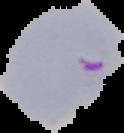

{
  "image_size": "124×133 pixels",
  "image_type": "segmented cell region with the area outside set to black",
  "preparation": "thin blood smear",
  "malaria_status": "parasitized"
}